Locate every blood parasite and identify its species.
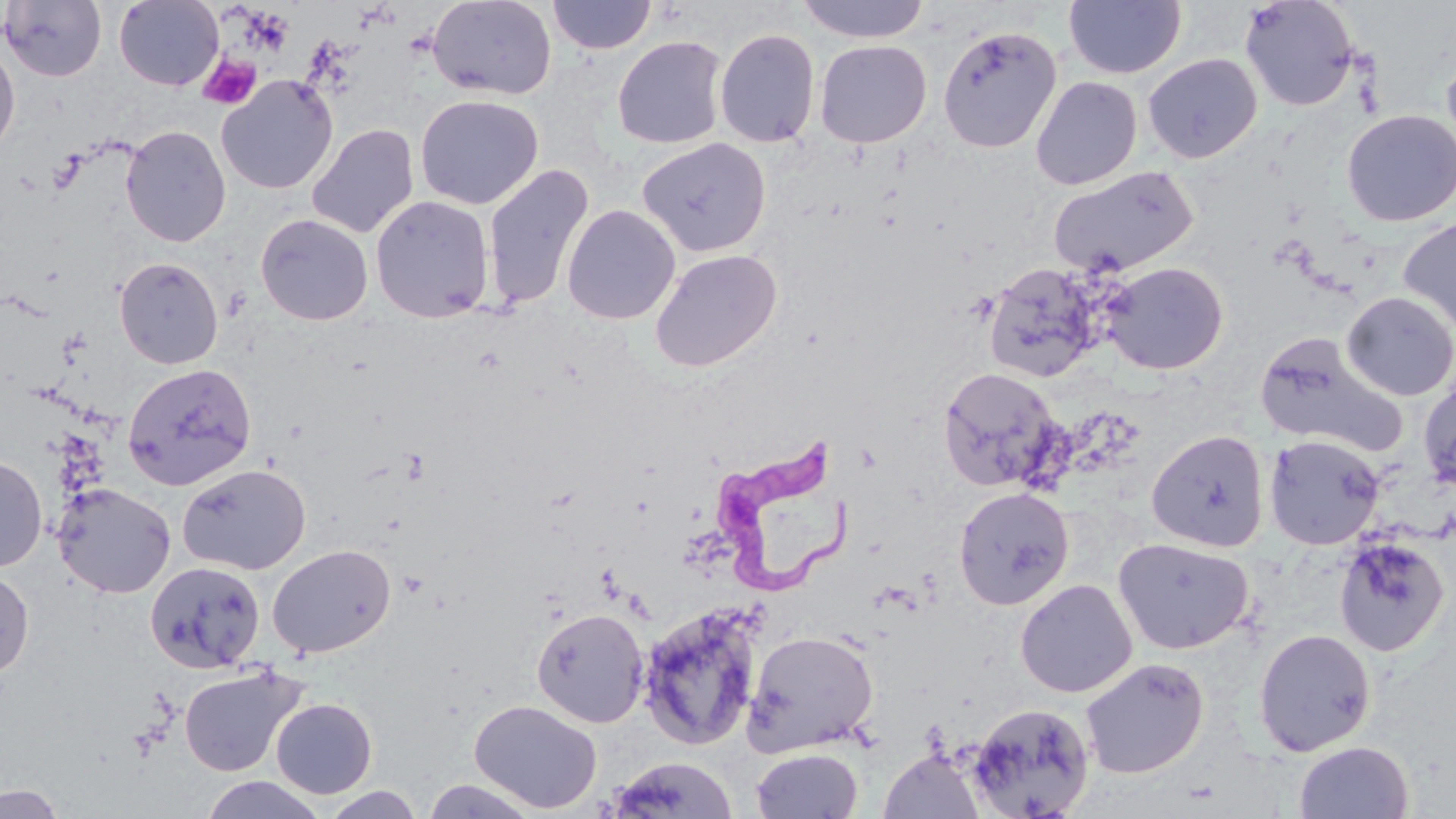

Approximate bounding boxes as [x1, y1, x2, y2] in pixels.
Trypanosoma brucei: [706, 430, 850, 599].
No Plasmodium falciparum, Plasmodium ovale, Plasmodium malariae, Plasmodium vivax, or Babesia divergens observed.

slide-level diagnosis = Trypanosoma brucei
stain = May-Grünwald-Giemsa
modality = light microscopy
magnification = 1000x
image size = 1456×819 pixels
field of view = one of a larger specimen
preparation = thin blood smear
platelet locations = approximate bounding boxes as [x1, y1, x2, y2] in pixels: [197, 54, 261, 110], [49, 153, 85, 194]
uninfected red blood cell locations = approximate bounding boxes as [x1, y1, x2, y2] in pixels: [114, 0, 223, 90], [427, 0, 556, 100], [546, 0, 657, 55], [797, 0, 930, 43], [1238, 0, 1360, 112], [1, 1, 107, 82], [1064, 1, 1186, 79], [937, 25, 1062, 153], [714, 28, 820, 148], [612, 35, 728, 149], [814, 40, 932, 148], [0, 43, 20, 156], [1441, 50, 1456, 161], [1142, 53, 1262, 163], [217, 75, 338, 194], [1030, 76, 1142, 190], [415, 95, 543, 209], [1341, 109, 1456, 227], [307, 123, 419, 239], [120, 125, 231, 247], [637, 137, 772, 258], [482, 164, 594, 311], [1048, 165, 1199, 278], [371, 195, 494, 323], [562, 204, 681, 325], [255, 213, 373, 326], [1397, 216, 1456, 336], [649, 249, 782, 372], [114, 257, 223, 369], [982, 262, 1107, 383], [1100, 262, 1229, 375], [1340, 291, 1456, 401], [1254, 332, 1408, 457], [123, 363, 257, 490], [937, 366, 1064, 493], [1418, 374, 1456, 494], [1146, 429, 1270, 552], [1264, 434, 1384, 550], [0, 454, 47, 572], [177, 463, 311, 575], [53, 482, 176, 598], [953, 486, 1075, 610], [1333, 534, 1452, 658], [1113, 537, 1254, 655], [267, 544, 396, 658], [144, 560, 265, 673], [0, 569, 35, 681], [1015, 578, 1138, 698], [637, 603, 764, 750], [531, 608, 649, 728], [1253, 627, 1376, 756], [743, 630, 879, 756], [1080, 657, 1209, 779], [178, 665, 306, 778], [271, 697, 378, 799], [469, 699, 602, 813], [966, 701, 1096, 819], [1294, 740, 1414, 819], [750, 748, 862, 819], [879, 749, 985, 819], [608, 756, 739, 819], [197, 775, 329, 819], [419, 777, 542, 818], [1, 784, 67, 819], [317, 785, 428, 818]